Assess for Plasmodium parasites.
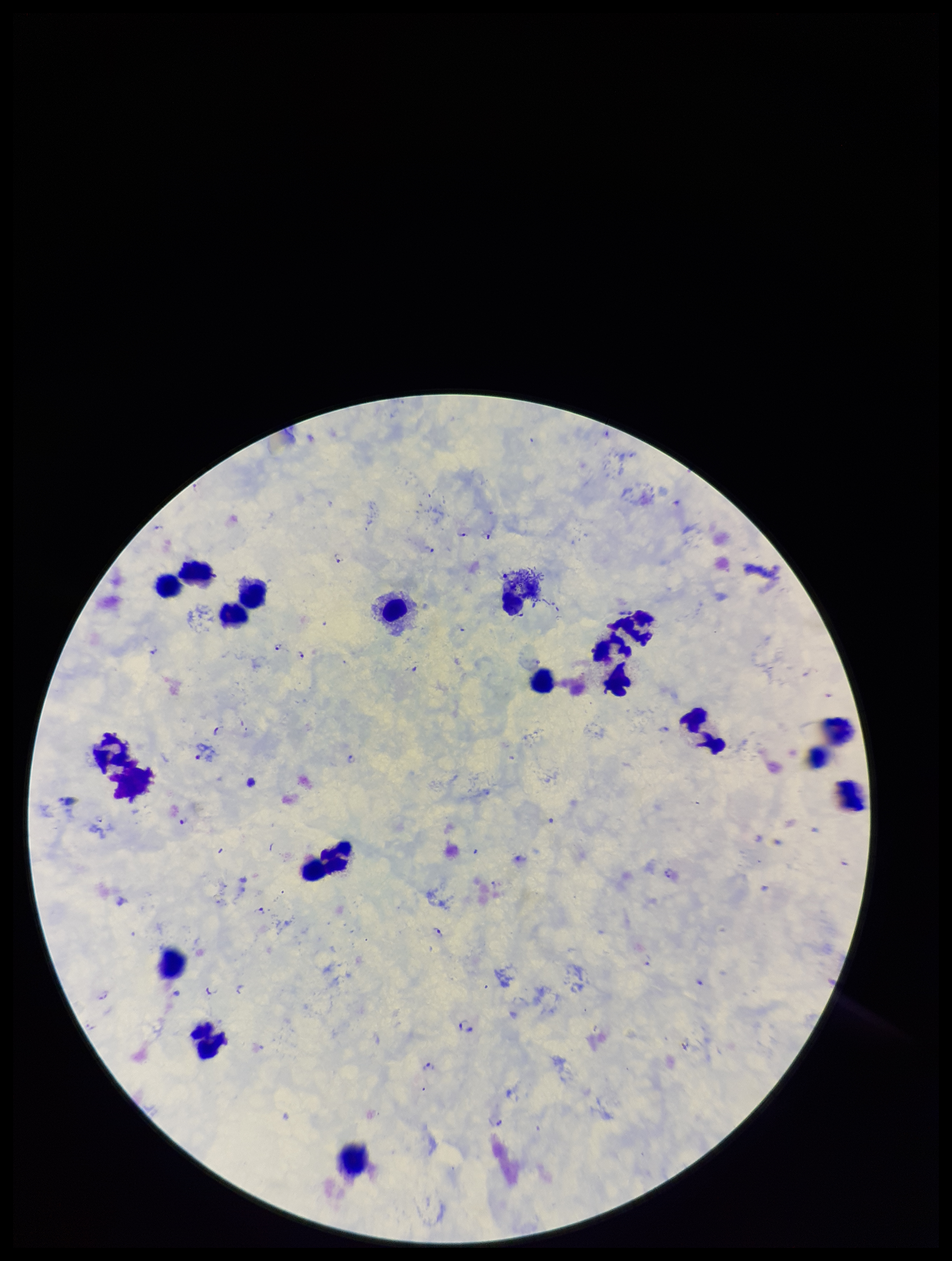
Seen.

parasite count = 19
preparation = thick smear
stain = Giemsa
capture = smartphone photograph through the microscope eyepiece
image size = 952×1261 pixels
leukocyte count = 20
species reported for this patient = Plasmodium falciparum
patient malaria status = infected
field of view = one from this slide